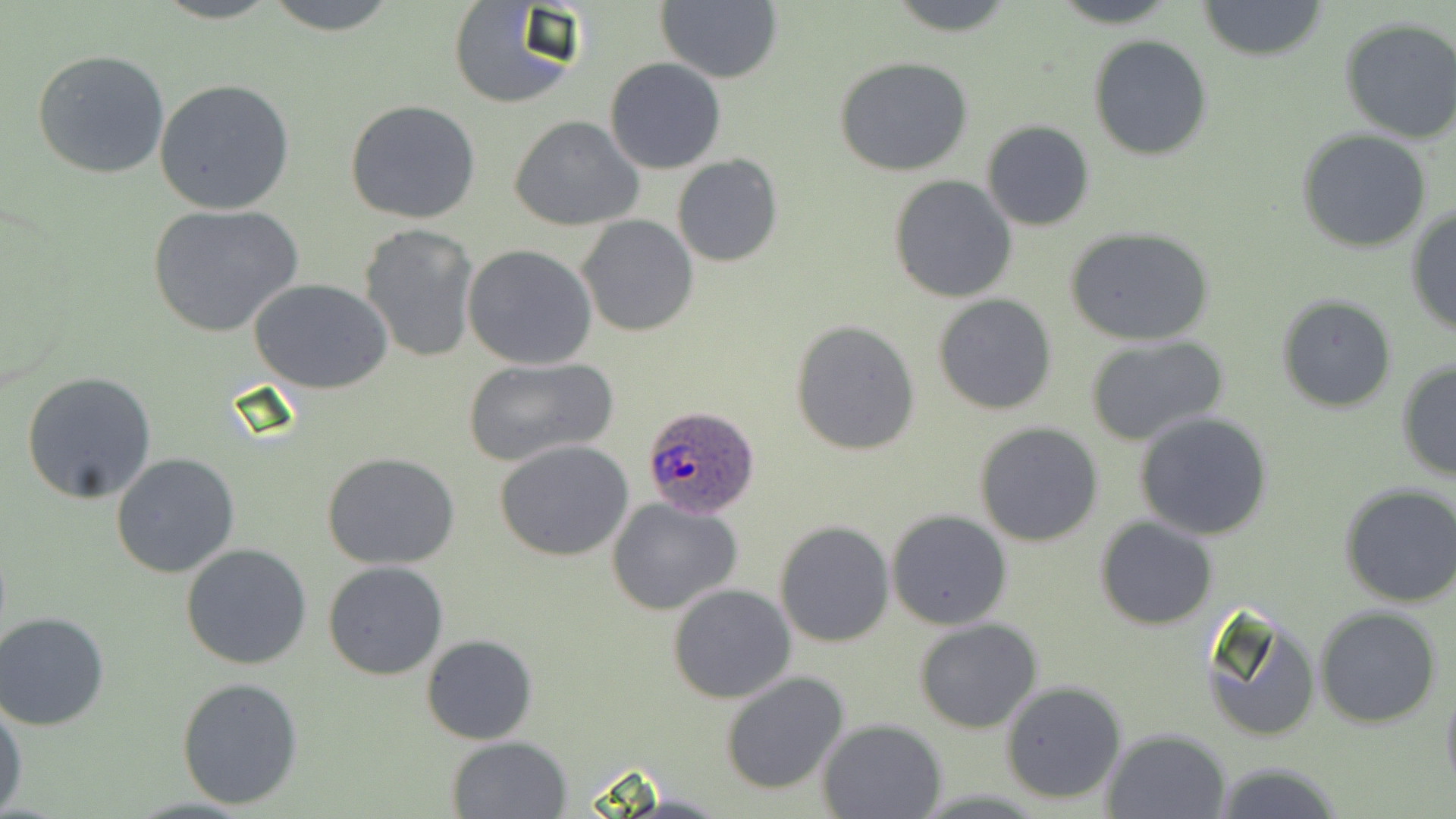 Approximate bounding boxes as (x1, y1, x2, y2) in pixels. Plasmodium ovale-infected red blood cell locations: (639, 404, 762, 518). Uninfected red blood cell locations: (261, 0, 402, 35), (446, 0, 580, 110), (655, 0, 782, 84), (884, 0, 1020, 36), (1198, 1, 1327, 61), (1339, 17, 1456, 143), (1089, 36, 1213, 159), (32, 48, 171, 179), (834, 56, 974, 176), (604, 57, 727, 174), (154, 78, 297, 216), (345, 99, 481, 224), (509, 115, 644, 233), (981, 120, 1095, 231), (1296, 128, 1432, 252), (671, 154, 782, 268), (888, 175, 1018, 303), (148, 204, 303, 337), (1406, 205, 1456, 338), (576, 215, 700, 338), (359, 223, 483, 363), (1068, 228, 1213, 346), (462, 244, 598, 370), (248, 277, 394, 392), (933, 294, 1058, 415), (1276, 295, 1396, 412), (790, 318, 921, 455), (1084, 335, 1229, 446), (460, 356, 617, 470), (1396, 360, 1455, 481), (21, 371, 158, 504), (1133, 411, 1275, 541), (973, 422, 1103, 546), (496, 440, 634, 562), (110, 451, 240, 578), (321, 451, 461, 570), (1338, 486, 1456, 607), (607, 496, 743, 614), (886, 509, 1012, 630), (1095, 517, 1217, 630), (773, 520, 894, 649), (180, 542, 313, 669), (323, 561, 450, 680), (668, 583, 797, 703), (1199, 603, 1323, 743), (1315, 606, 1441, 728), (1, 610, 115, 731), (914, 619, 1043, 734), (422, 634, 538, 744), (719, 671, 850, 797), (177, 676, 305, 810), (1440, 677, 1456, 798), (1000, 680, 1127, 806), (0, 696, 25, 816), (817, 718, 949, 818), (1102, 727, 1234, 818), (444, 736, 573, 819), (1210, 762, 1346, 819). Slide-level diagnosis: Plasmodium ovale. Image is 1456×819 pixels. Thin blood film. May-Grünwald-Giemsa-stained preparation. One field of a larger specimen. Captured at 1000x magnification. Optical microscopy.